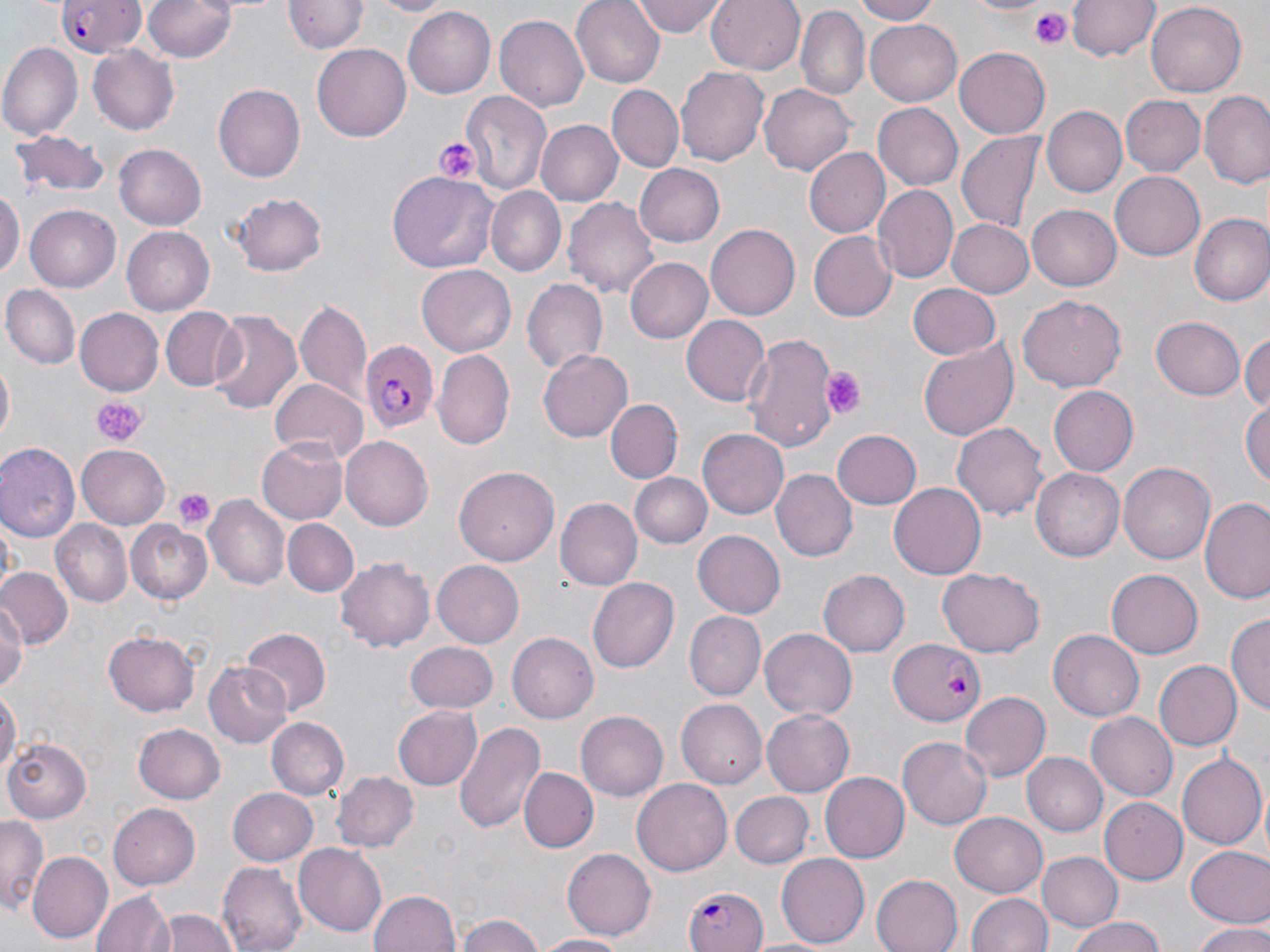

slide-level diagnosis = Plasmodium falciparum
stain = May-Grünwald-Giemsa
image size = 1270×952 pixels
field of view = single
magnification = 1000x
uninfected red blood cell locations = approximate bounding boxes as [x1, y1, x2, y2] in pixels: [142, 0, 239, 63], [364, 0, 453, 16], [573, 0, 664, 87], [632, 0, 726, 38], [706, 0, 806, 75], [855, 0, 941, 24], [966, 0, 1052, 17], [285, 1, 367, 55], [1069, 1, 1157, 61], [1148, 2, 1246, 95], [403, 7, 495, 98], [796, 8, 869, 102], [496, 13, 588, 112], [866, 15, 962, 102], [0, 43, 81, 140], [312, 44, 411, 142], [89, 46, 179, 135], [955, 48, 1051, 139], [675, 64, 769, 166], [214, 83, 306, 181], [760, 83, 856, 174], [607, 85, 684, 171], [460, 88, 553, 198], [1200, 91, 1270, 188], [1121, 95, 1207, 176], [872, 102, 964, 190], [1041, 106, 1127, 197], [535, 120, 623, 206], [9, 132, 109, 202], [958, 132, 1045, 234], [114, 143, 207, 230], [806, 146, 891, 237], [634, 164, 724, 247], [1110, 170, 1206, 260], [391, 172, 498, 272], [872, 185, 957, 284], [0, 186, 22, 283], [489, 187, 565, 275], [232, 191, 328, 277], [564, 196, 659, 300], [25, 205, 119, 291], [1027, 205, 1122, 290], [1190, 214, 1270, 307], [947, 219, 1035, 297], [706, 223, 800, 319], [121, 226, 214, 315], [808, 231, 896, 322], [627, 258, 712, 341], [416, 265, 515, 356], [520, 278, 608, 374], [2, 283, 80, 371], [908, 283, 1002, 360], [1017, 294, 1128, 392], [295, 298, 370, 403], [158, 307, 241, 391], [76, 308, 162, 394], [208, 309, 304, 413], [680, 315, 770, 407], [1151, 317, 1245, 401], [1243, 331, 1270, 413], [743, 332, 838, 453], [918, 341, 1019, 441], [434, 349, 515, 448], [538, 349, 631, 441], [1, 362, 14, 444], [266, 379, 368, 466], [1048, 386, 1137, 475], [605, 398, 682, 481], [1242, 399, 1270, 493], [952, 420, 1049, 520], [699, 428, 789, 518], [832, 429, 921, 510], [259, 434, 348, 524], [341, 436, 434, 530], [0, 443, 79, 540], [76, 445, 171, 528], [1120, 462, 1215, 564], [455, 465, 557, 566], [1032, 467, 1127, 561], [772, 469, 858, 562], [631, 472, 712, 549], [890, 481, 989, 580], [205, 496, 290, 590], [1200, 497, 1270, 607], [556, 498, 641, 590], [50, 517, 131, 609], [126, 519, 212, 604], [283, 519, 358, 597], [694, 531, 785, 618], [336, 557, 435, 654], [431, 559, 525, 651], [0, 567, 71, 648], [937, 567, 1044, 659], [818, 569, 910, 657], [1105, 570, 1201, 659], [588, 577, 678, 673], [0, 597, 24, 696], [685, 611, 765, 701], [1228, 614, 1269, 719], [761, 627, 858, 719], [1049, 627, 1146, 720], [242, 629, 330, 714], [104, 632, 199, 716], [506, 632, 598, 723], [405, 641, 499, 712], [1153, 660, 1242, 752], [205, 661, 290, 748], [0, 685, 19, 782], [961, 691, 1051, 781], [676, 698, 767, 790], [392, 706, 482, 790], [763, 707, 858, 797], [577, 709, 667, 799], [1087, 712, 1178, 800], [266, 717, 350, 800], [453, 721, 544, 835], [134, 724, 225, 804], [898, 736, 992, 829], [5, 739, 96, 823], [1023, 752, 1108, 835], [1178, 752, 1268, 849], [520, 767, 597, 851], [819, 771, 909, 864], [334, 772, 417, 853], [632, 779, 732, 876], [229, 787, 317, 865], [730, 792, 812, 867], [1101, 797, 1186, 883], [107, 802, 200, 891], [950, 812, 1047, 898], [0, 815, 47, 917], [294, 842, 387, 935], [1186, 845, 1270, 928], [562, 847, 657, 941], [27, 850, 113, 943], [1039, 851, 1121, 932], [775, 853, 870, 948], [217, 861, 307, 952], [871, 873, 961, 952], [369, 887, 463, 952], [92, 888, 174, 952], [964, 892, 1052, 952], [156, 908, 238, 952], [455, 913, 549, 952], [1063, 918, 1173, 952], [1192, 924, 1270, 952], [535, 933, 631, 952]
preparation = thin blood film
Plasmodium falciparum-infected red blood cell locations = approximate bounding boxes as [x1, y1, x2, y2] in pixels: [56, 1, 147, 57], [365, 342, 440, 436], [887, 639, 987, 726], [680, 886, 767, 952]
platelet locations = approximate bounding boxes as [x1, y1, x2, y2] in pixels: [1030, 10, 1071, 48], [433, 137, 478, 183], [825, 367, 866, 417], [92, 397, 144, 447], [172, 489, 212, 531]
modality = light microscopy